Outline each blood parasite and name the species.
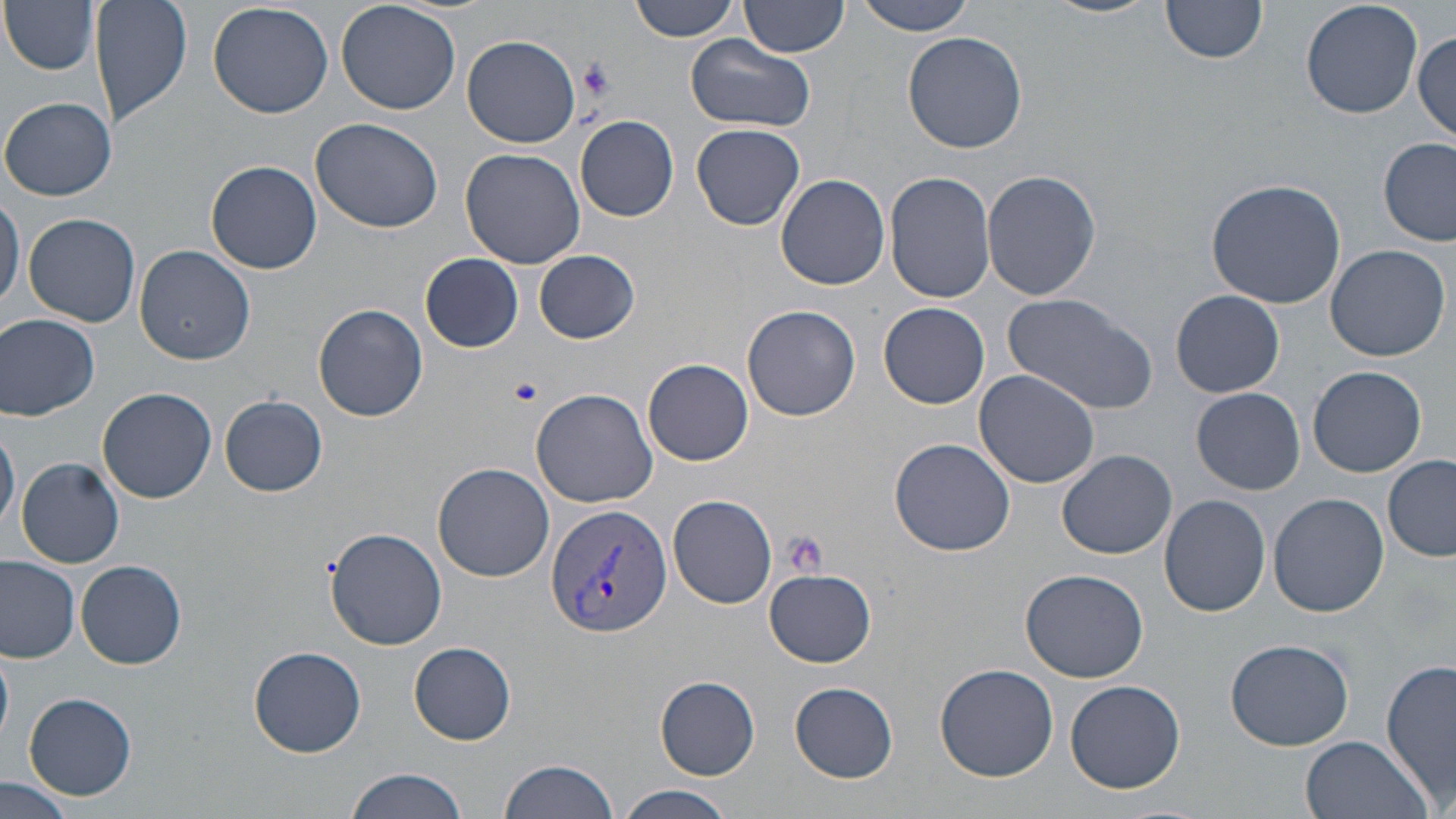

Approximate bounding boxes as [x1, y1, x2, y2] in pixels.
Plasmodium vivax-infected red blood cells: [546, 503, 673, 639].
No Plasmodium falciparum, Plasmodium ovale, Plasmodium malariae, Babesia divergens, or Trypanosoma brucei observed.

Summary:
  - Platelet locations: [576, 58, 616, 98], [506, 377, 543, 407], [781, 531, 827, 578]
  - Uninfected red blood cell locations: [1, 0, 100, 75], [90, 0, 192, 130], [337, 0, 461, 115], [628, 0, 744, 41], [738, 0, 848, 60], [851, 0, 980, 35], [1047, 0, 1157, 19], [1300, 0, 1424, 119], [207, 1, 333, 118], [1159, 1, 1266, 66], [904, 30, 1027, 154], [1412, 32, 1455, 144], [462, 35, 582, 148], [686, 35, 815, 132], [2, 97, 117, 201], [574, 114, 679, 223], [311, 118, 444, 235], [691, 123, 805, 231], [1377, 139, 1455, 246], [459, 147, 585, 269], [206, 160, 322, 274], [885, 170, 996, 304], [982, 170, 1101, 302], [776, 174, 890, 290], [1206, 178, 1348, 309], [0, 188, 23, 319], [23, 212, 142, 327], [1324, 243, 1451, 361], [136, 246, 255, 365], [534, 249, 641, 344], [421, 254, 525, 352], [1171, 290, 1285, 399], [1002, 294, 1159, 414], [313, 303, 428, 422], [879, 303, 989, 409], [742, 304, 861, 423], [1, 313, 100, 421], [644, 359, 753, 465], [1307, 365, 1428, 478], [974, 370, 1100, 488], [98, 386, 216, 503], [530, 387, 658, 507], [1191, 387, 1306, 496], [220, 396, 327, 496], [0, 422, 20, 538], [889, 437, 1019, 556], [1058, 449, 1176, 559], [1383, 456, 1456, 561], [16, 458, 126, 568], [433, 462, 554, 581], [1268, 493, 1388, 616], [666, 494, 777, 609], [1158, 494, 1270, 616], [327, 527, 445, 649], [0, 556, 80, 662], [77, 559, 187, 669], [764, 567, 877, 667], [1019, 567, 1150, 680], [1226, 638, 1355, 750], [409, 642, 517, 745], [0, 647, 15, 742], [250, 647, 367, 757], [1383, 657, 1456, 809], [934, 662, 1060, 780], [654, 676, 761, 780], [1065, 680, 1186, 793], [789, 681, 899, 782], [22, 692, 137, 801], [1301, 733, 1430, 819], [496, 757, 623, 819], [344, 767, 473, 819], [0, 777, 81, 819], [620, 785, 736, 819]
  - Slide-level diagnosis: Plasmodium vivax
  - Image size: 1456×819 pixels
  - Stain: May-Grünwald-Giemsa
  - Modality: optical microscopy
  - Preparation: thin blood smear
  - Magnification: 1000x
  - Field of view: one of a larger specimen